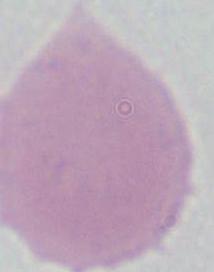
identification = red blood cell
magnification = 1000x
modality = micrograph